Name the blood parasite species.
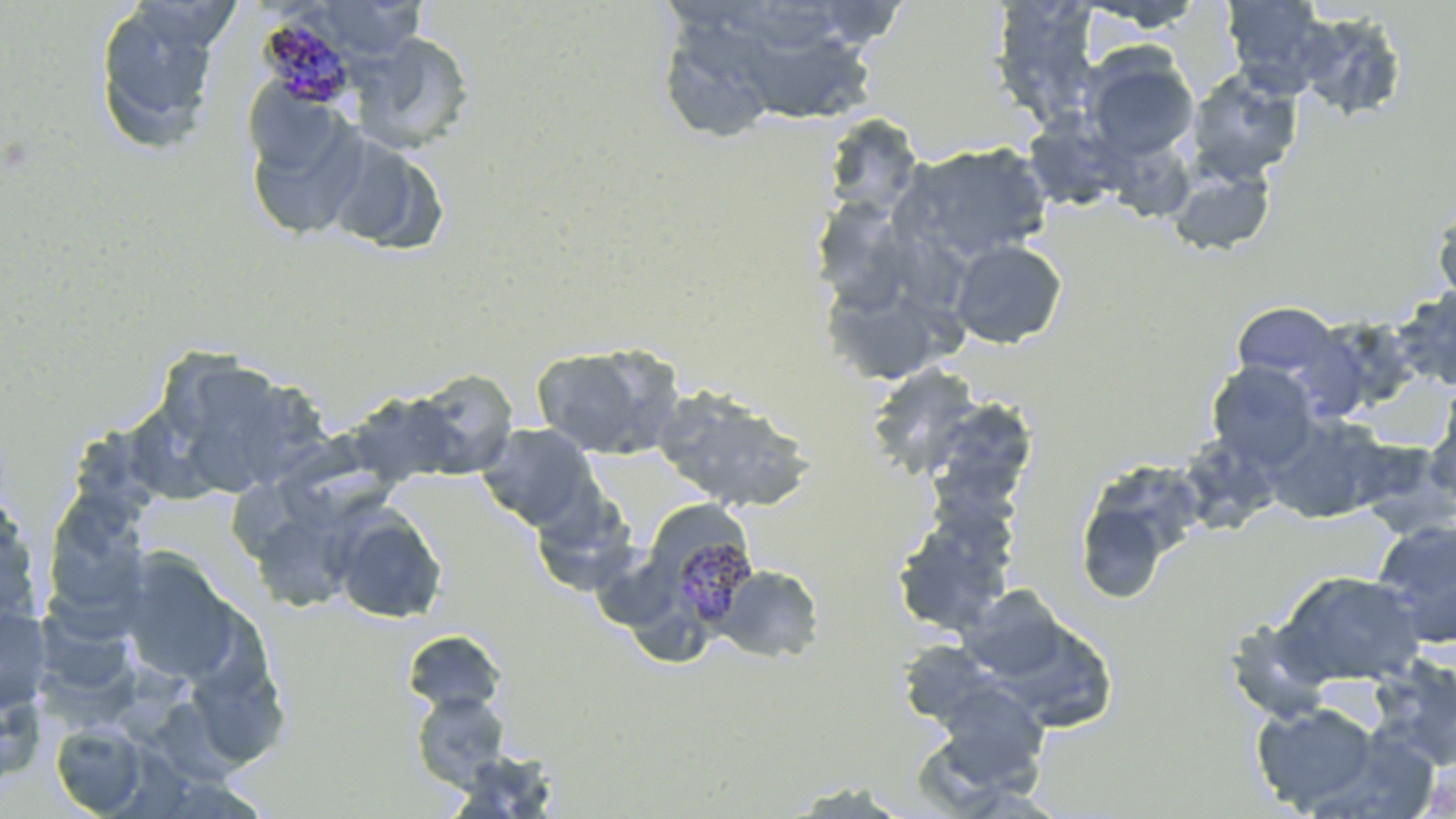
Plasmodium malariae.

image size = 1456×819 pixels
uninfected red blood cell locations = approximate bounding boxes as [x1, y1, x2, y2] in pixels: [93, 0, 224, 151], [315, 0, 426, 57], [988, 0, 1103, 131], [1219, 0, 1332, 94], [1076, 1, 1208, 33], [805, 2, 912, 48], [1293, 10, 1409, 123], [657, 14, 784, 143], [351, 32, 476, 153], [757, 39, 875, 121], [1080, 47, 1199, 161], [1185, 68, 1303, 183], [244, 94, 369, 241], [1015, 103, 1118, 211], [821, 113, 924, 219], [896, 142, 1052, 264], [1106, 147, 1195, 234], [1167, 165, 1276, 257], [812, 191, 916, 317], [1432, 199, 1456, 309], [950, 240, 1067, 349], [822, 274, 933, 368], [1393, 287, 1456, 391], [1231, 302, 1343, 386], [530, 344, 681, 461], [154, 358, 303, 497], [1207, 362, 1318, 468], [865, 364, 986, 479], [410, 368, 520, 477], [346, 385, 462, 493], [652, 385, 815, 513], [927, 398, 1038, 510], [1423, 402, 1456, 511], [1263, 414, 1389, 523], [477, 422, 598, 530], [286, 432, 403, 534], [1176, 432, 1283, 536], [1351, 438, 1454, 537], [1075, 484, 1178, 607], [42, 489, 154, 627], [531, 489, 639, 596], [0, 494, 42, 633], [245, 506, 358, 613], [331, 507, 447, 624], [891, 514, 1016, 637], [1371, 517, 1456, 647], [116, 550, 245, 687], [715, 565, 824, 663], [1274, 570, 1428, 688], [958, 586, 1071, 681], [0, 605, 52, 713], [1223, 615, 1338, 724], [402, 630, 507, 716], [897, 639, 998, 728], [1368, 656, 1456, 772], [194, 671, 291, 769], [0, 677, 47, 792], [929, 682, 1051, 793], [411, 690, 511, 789], [1251, 702, 1380, 813], [150, 703, 248, 789], [51, 722, 148, 816], [448, 750, 560, 816], [779, 781, 914, 817]
magnification = 1000x
stain = May-Grünwald-Giemsa
preparation = thin blood smear
modality = optical microscopy
Plasmodium malariae-infected red blood cell locations = approximate bounding boxes as [x1, y1, x2, y2] in pixels: [257, 15, 358, 109], [670, 534, 759, 628]
field of view = one of a larger specimen